Assess this cell for malaria.
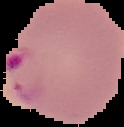

Parasitized.

image size = 124×127 pixels
image type = segmented cell region with the area outside set to black
preparation = thin blood smear